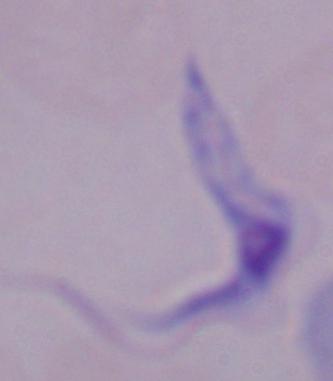
Summary:
  - Modality: photomicrograph
  - Identification: trypanosome
  - Magnification: 1000x